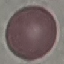
result: negative for malaria parasites
preparation: thin blood film
stain: Giemsa
image_type: cell patch, automatically extracted from a larger field of view and resized to 64 × 64 pixels
capture: smartphone through the microscope eyepiece